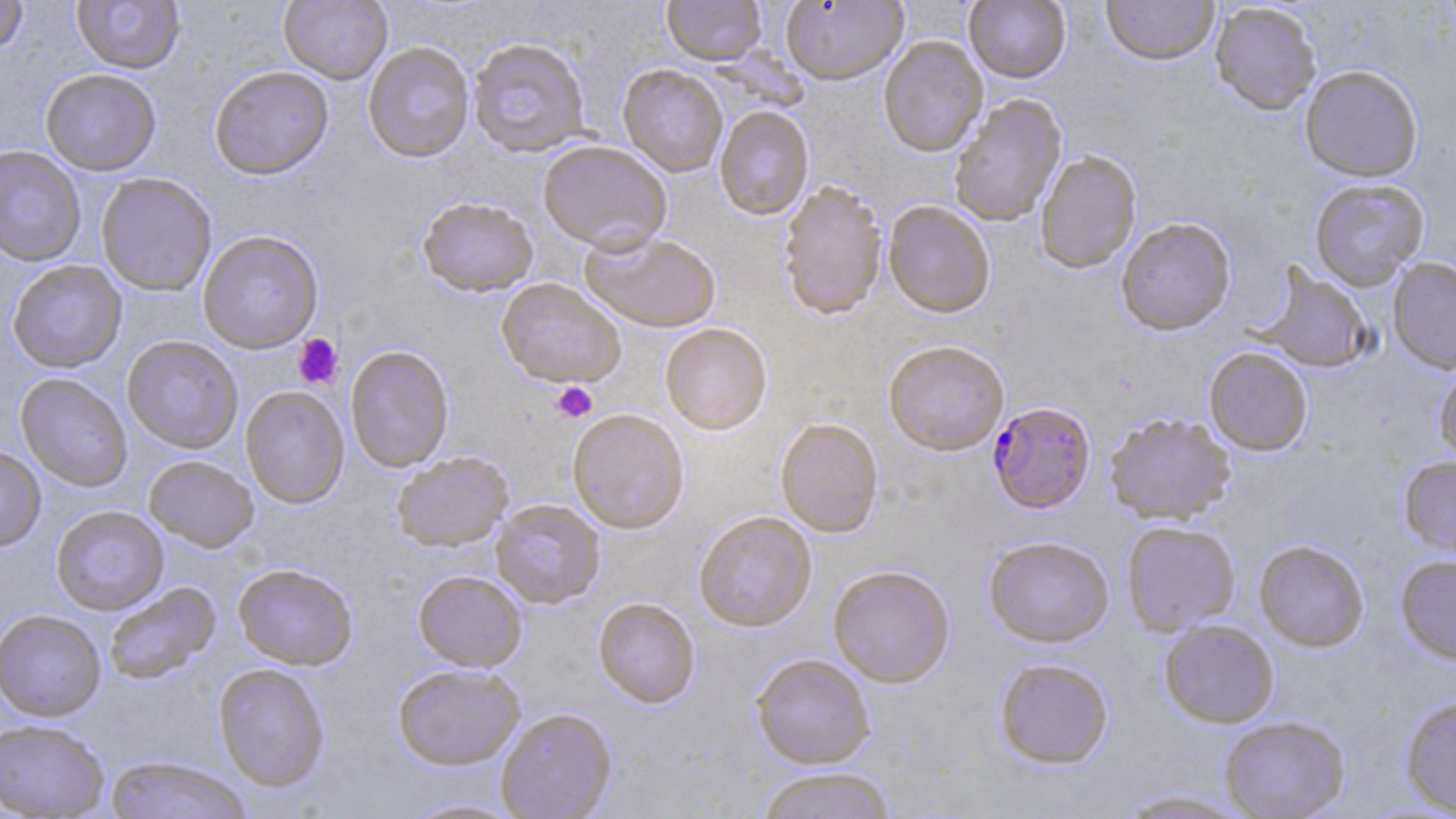

{
  "slide_level_diagnosis": "Plasmodium falciparum",
  "stain": "May-Grünwald-Giemsa",
  "magnification": "1000x",
  "field_of_view": "one of a larger specimen",
  "image_size": "1456×819 pixels",
  "modality": "optical microscopy",
  "plasmodium_falciparum_infected_red_blood_cell_locations": "approximate bounding boxes as [x1, y1, x2, y2] in pixels: [988, 402, 1096, 513]",
  "preparation": "thin blood smear",
  "platelet_locations": "approximate bounding boxes as [x1, y1, x2, y2] in pixels: [293, 334, 343, 389], [551, 381, 597, 422]",
  "uninfected_red_blood_cell_locations": "approximate bounding boxes as [x1, y1, x2, y2] in pixels: [279, 0, 393, 84], [662, 0, 766, 65], [780, 0, 908, 85], [964, 0, 1071, 83], [1102, 0, 1219, 65], [0, 1, 29, 55], [72, 1, 185, 73], [1210, 3, 1322, 115], [878, 35, 988, 157], [467, 37, 591, 157], [363, 42, 474, 162], [618, 64, 728, 177], [209, 65, 334, 180], [1300, 65, 1423, 182], [40, 68, 161, 175], [949, 94, 1067, 227], [714, 105, 814, 220], [538, 140, 672, 253], [0, 145, 86, 267], [1035, 150, 1141, 274], [96, 172, 217, 296], [1309, 178, 1429, 290], [778, 179, 887, 320], [417, 196, 539, 296], [883, 201, 995, 318], [1116, 217, 1236, 336], [580, 229, 722, 333], [197, 230, 324, 354], [1388, 256, 1456, 374], [7, 260, 127, 373], [1257, 266, 1375, 374], [496, 278, 625, 388], [660, 323, 772, 434], [122, 335, 243, 453], [883, 340, 1009, 455], [345, 344, 455, 472], [1204, 347, 1313, 456], [1433, 359, 1456, 464], [16, 373, 133, 492], [240, 385, 350, 508], [567, 409, 689, 533], [1104, 412, 1236, 525], [775, 418, 884, 537], [0, 445, 46, 551], [391, 451, 513, 551], [144, 455, 259, 552], [1399, 455, 1456, 560], [491, 499, 606, 609], [51, 506, 168, 615], [694, 511, 817, 632], [1121, 521, 1240, 636], [983, 536, 1114, 649], [1254, 540, 1369, 652], [1395, 554, 1456, 664], [233, 563, 358, 670], [828, 566, 955, 687], [413, 570, 527, 671], [104, 581, 221, 685], [593, 597, 700, 708], [0, 610, 107, 722], [1158, 620, 1279, 728], [751, 653, 875, 769], [994, 658, 1113, 769], [213, 663, 330, 792], [392, 663, 525, 769], [1400, 694, 1456, 815], [496, 708, 616, 819], [1219, 716, 1350, 818], [0, 718, 109, 818], [104, 756, 253, 819], [756, 767, 897, 819], [1115, 789, 1252, 818], [395, 797, 530, 818]"
}